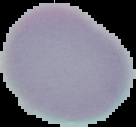

Summary:
  - Malaria status: uninfected
  - Image type: segmented cell region with the area outside set to black
  - Preparation: thin blood film
  - Image size: 136×127 pixels